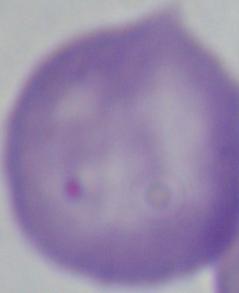
magnification = 1000x
modality = micrograph
identification = Babesia